Name the parasite shown.
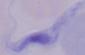

This is a trypanosome.

Summary:
  - Modality: photomicrograph
  - Magnification: 1000x